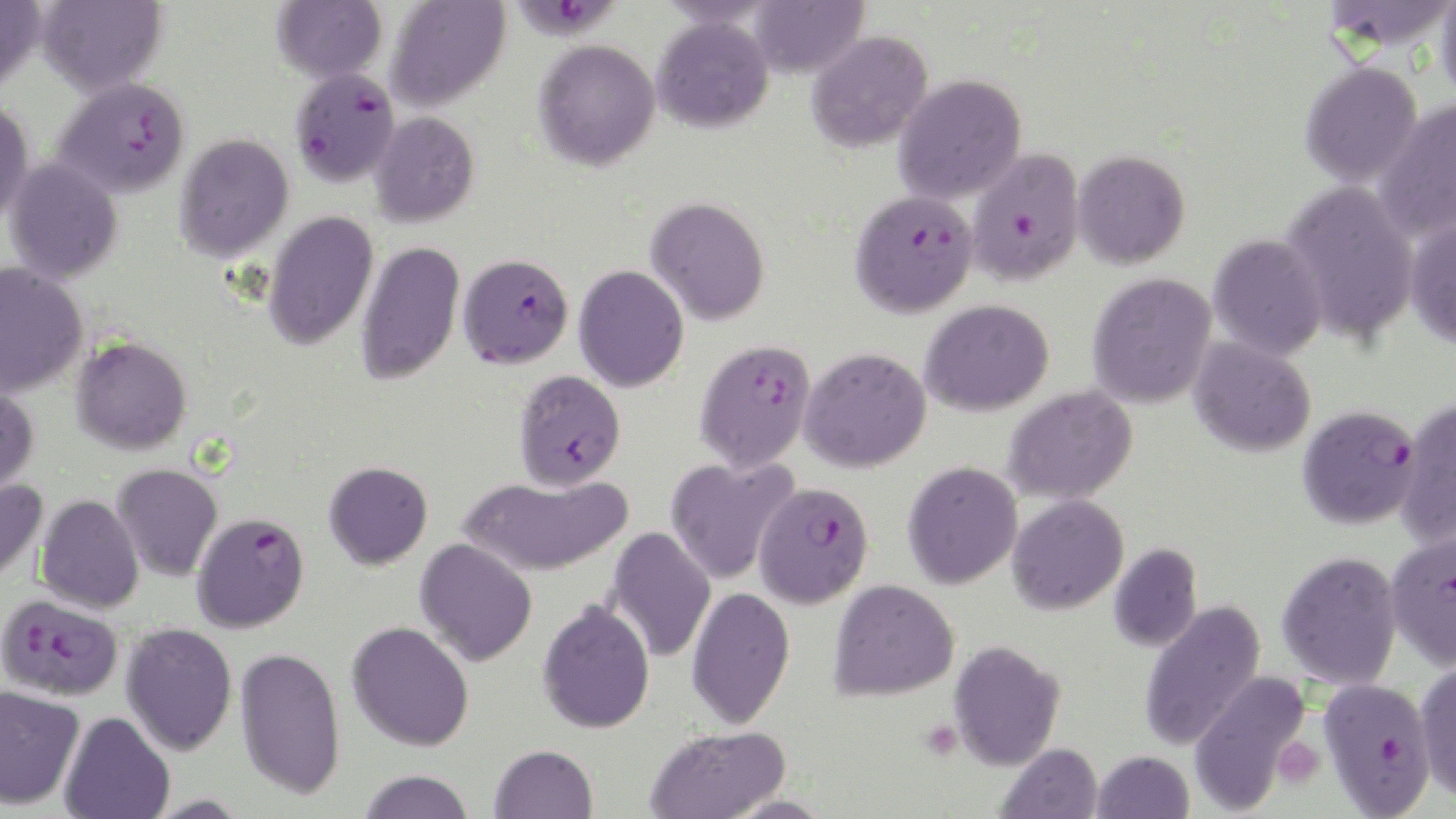

Summary:
  - Coordinate format: approximate bounding boxes as (x1,y1)-(x2,y2) corner pairs in pixels
  - Plasmodium falciparum-infected red blood cell locations: (511,0)-(625,46), (289,66)-(400,186), (54,77)-(190,198), (968,148)-(1083,286), (850,188)-(980,318), (457,253)-(574,368), (693,339)-(817,473), (514,369)-(626,490), (1297,405)-(1423,530), (752,480)-(874,608), (191,511)-(310,633), (1385,530)-(1456,672), (0,596)-(119,704), (1317,678)-(1436,818)
  - Platelet locations: (1272,738)-(1325,788)
  - Uninfected red blood cell locations: (0,0)-(45,91), (35,0)-(169,96), (270,0)-(387,83), (385,0)-(510,112), (746,0)-(868,77), (1329,0)-(1456,58), (1436,0)-(1456,104), (651,15)-(774,133), (806,30)-(933,152), (533,39)-(660,171), (1300,60)-(1423,187), (893,74)-(1027,204), (0,98)-(34,226), (1374,99)-(1456,242), (369,111)-(480,227), (174,133)-(294,262), (1072,149)-(1190,269), (4,158)-(123,284), (1280,181)-(1420,343), (645,197)-(770,326), (263,210)-(380,351), (1405,216)-(1456,349), (1208,233)-(1328,360), (355,240)-(465,385), (0,262)-(88,398), (573,265)-(689,392), (1086,272)-(1217,409), (919,299)-(1054,416), (71,336)-(192,454), (1189,337)-(1316,457), (799,347)-(932,473), (0,385)-(39,498), (1003,385)-(1138,504), (1395,397)-(1456,549), (665,455)-(799,586), (902,460)-(1022,589), (324,461)-(433,569), (112,463)-(223,581), (460,473)-(631,576), (0,478)-(48,585), (35,494)-(144,614), (1007,495)-(1129,615), (606,526)-(716,663), (415,538)-(538,666), (1109,543)-(1203,652), (1276,550)-(1402,689), (828,578)-(960,701), (686,586)-(795,729), (537,600)-(655,734), (1138,600)-(1267,751), (347,621)-(475,751), (121,622)-(238,755), (948,640)-(1066,771), (235,645)-(346,799), (1414,658)-(1456,802), (1188,669)-(1313,814), (0,685)-(83,810), (60,711)-(175,819), (644,724)-(791,819), (995,742)-(1103,819), (489,744)-(598,819), (1091,750)-(1194,818), (358,769)-(476,819)
  - Slide-level diagnosis: Plasmodium falciparum
  - Magnification: 1000x
  - Preparation: thin blood smear
  - Image size: 1456×819 pixels
  - Modality: light microscopy
  - Field of view: single
  - Stain: May-Grünwald-Giemsa